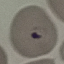
{
  "result": "malaria parasites detected",
  "preparation": "thin blood film",
  "image_type": "cell patch, automatically extracted from a larger field of view and resized to 64 × 64 pixels",
  "capture": "smartphone through the microscope eyepiece",
  "stain": "Giemsa"
}